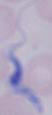
Photomicrograph. Captured at 1000x magnification. A trypanosome is seen.